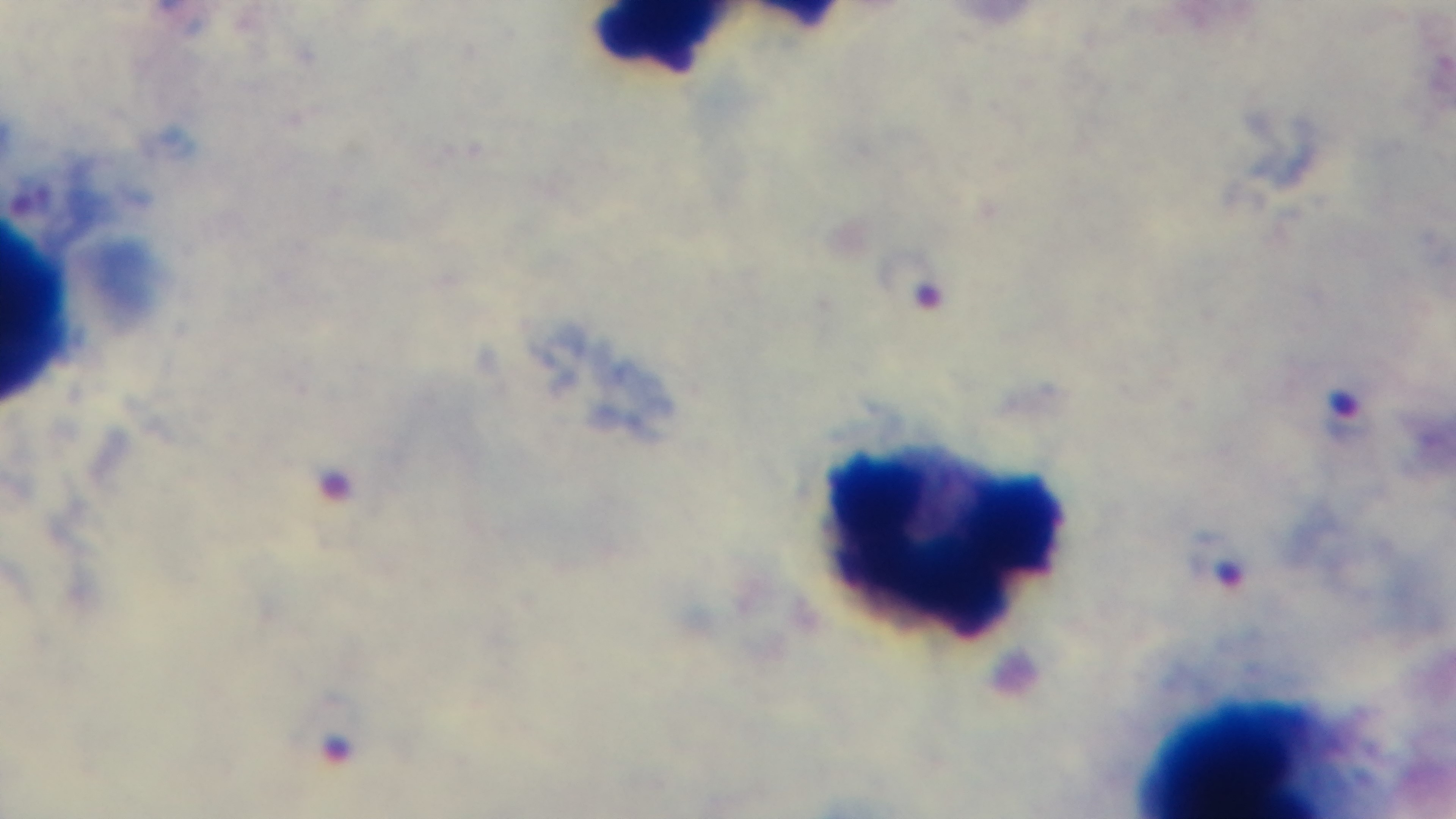

Summary:
  - Objective: 100x oil immersion
  - Modality: light microscopy
  - Field of view: one from the slide
  - Stain: Giemsa
  - Preparation: thick smear
  - Capture: mounted 4K digital camera
  - Malaria status: positive